Locate every Babesia divergens-infected red blood cell.
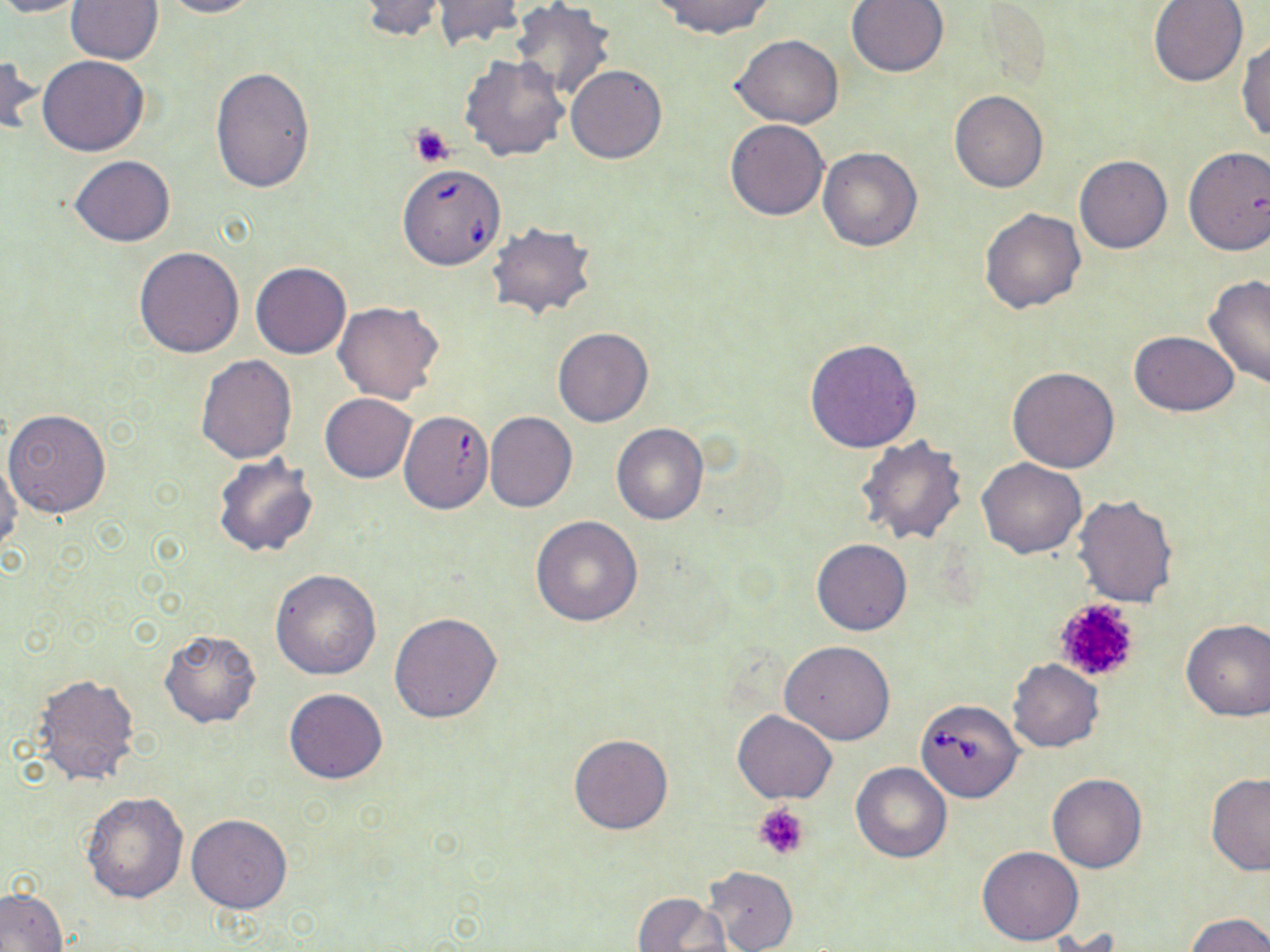

Approximate bounding boxes as named x1/y1/x2/y2 corners in pixels.
Babesia divergens-infected red blood cells: (x1=397, y1=162, x2=507, y2=270), (x1=915, y1=699, x2=1024, y2=802).

Platelet locations: (x1=410, y1=123, x2=455, y2=167), (x1=1051, y1=596, x2=1142, y2=683), (x1=753, y1=803, x2=811, y2=862). Uninfected red blood cell locations: (x1=0, y1=0, x2=90, y2=18), (x1=66, y1=0, x2=163, y2=64), (x1=161, y1=0, x2=263, y2=18), (x1=354, y1=0, x2=450, y2=42), (x1=650, y1=0, x2=776, y2=39), (x1=845, y1=0, x2=950, y2=78), (x1=430, y1=1, x2=526, y2=51), (x1=510, y1=1, x2=616, y2=102), (x1=1148, y1=1, x2=1248, y2=87), (x1=731, y1=35, x2=844, y2=128), (x1=1236, y1=37, x2=1270, y2=140), (x1=1, y1=53, x2=43, y2=139), (x1=459, y1=54, x2=570, y2=160), (x1=37, y1=56, x2=149, y2=156), (x1=565, y1=65, x2=667, y2=164), (x1=211, y1=68, x2=315, y2=194), (x1=949, y1=90, x2=1049, y2=193), (x1=724, y1=119, x2=830, y2=221), (x1=1183, y1=146, x2=1270, y2=256), (x1=818, y1=147, x2=922, y2=251), (x1=70, y1=155, x2=175, y2=247), (x1=1074, y1=155, x2=1172, y2=253), (x1=979, y1=206, x2=1088, y2=314), (x1=486, y1=221, x2=597, y2=322), (x1=134, y1=247, x2=244, y2=357), (x1=251, y1=262, x2=351, y2=359), (x1=1202, y1=275, x2=1270, y2=390), (x1=333, y1=302, x2=444, y2=405), (x1=552, y1=328, x2=654, y2=427), (x1=1129, y1=330, x2=1240, y2=416), (x1=805, y1=338, x2=921, y2=452), (x1=196, y1=354, x2=297, y2=463), (x1=1008, y1=366, x2=1121, y2=472), (x1=320, y1=393, x2=416, y2=483), (x1=3, y1=410, x2=111, y2=517), (x1=401, y1=412, x2=492, y2=517), (x1=484, y1=412, x2=577, y2=513), (x1=611, y1=422, x2=709, y2=525), (x1=854, y1=435, x2=968, y2=545), (x1=210, y1=453, x2=320, y2=558), (x1=0, y1=457, x2=23, y2=559), (x1=977, y1=458, x2=1086, y2=559), (x1=1071, y1=493, x2=1180, y2=607), (x1=530, y1=516, x2=643, y2=625), (x1=812, y1=539, x2=911, y2=636), (x1=270, y1=570, x2=382, y2=679), (x1=390, y1=612, x2=501, y2=722), (x1=1180, y1=618, x2=1270, y2=720), (x1=158, y1=628, x2=262, y2=728), (x1=779, y1=642, x2=894, y2=745), (x1=1007, y1=657, x2=1104, y2=752), (x1=32, y1=673, x2=141, y2=787), (x1=284, y1=688, x2=389, y2=784), (x1=732, y1=709, x2=838, y2=805), (x1=568, y1=734, x2=674, y2=835), (x1=851, y1=763, x2=951, y2=863), (x1=1047, y1=774, x2=1147, y2=873), (x1=1205, y1=775, x2=1270, y2=876), (x1=81, y1=792, x2=187, y2=903), (x1=186, y1=813, x2=294, y2=913), (x1=977, y1=846, x2=1084, y2=946), (x1=702, y1=865, x2=797, y2=952), (x1=1, y1=888, x2=67, y2=952), (x1=633, y1=891, x2=731, y2=952), (x1=1185, y1=913, x2=1270, y2=951). Slide-level diagnosis: Babesia divergens. Captured at 1000x magnification. Light microscopy. One field of a larger specimen. Thin blood smear. May-Grünwald-Giemsa stain. Image is 1270×952 pixels.